Classify this cell by malaria status.
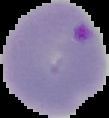
Parasitized.

preparation = thin blood film
image size = 109×118 pixels
image type = segmented cell region on a black background